Outline each Plasmodium ovale-infected red blood cell.
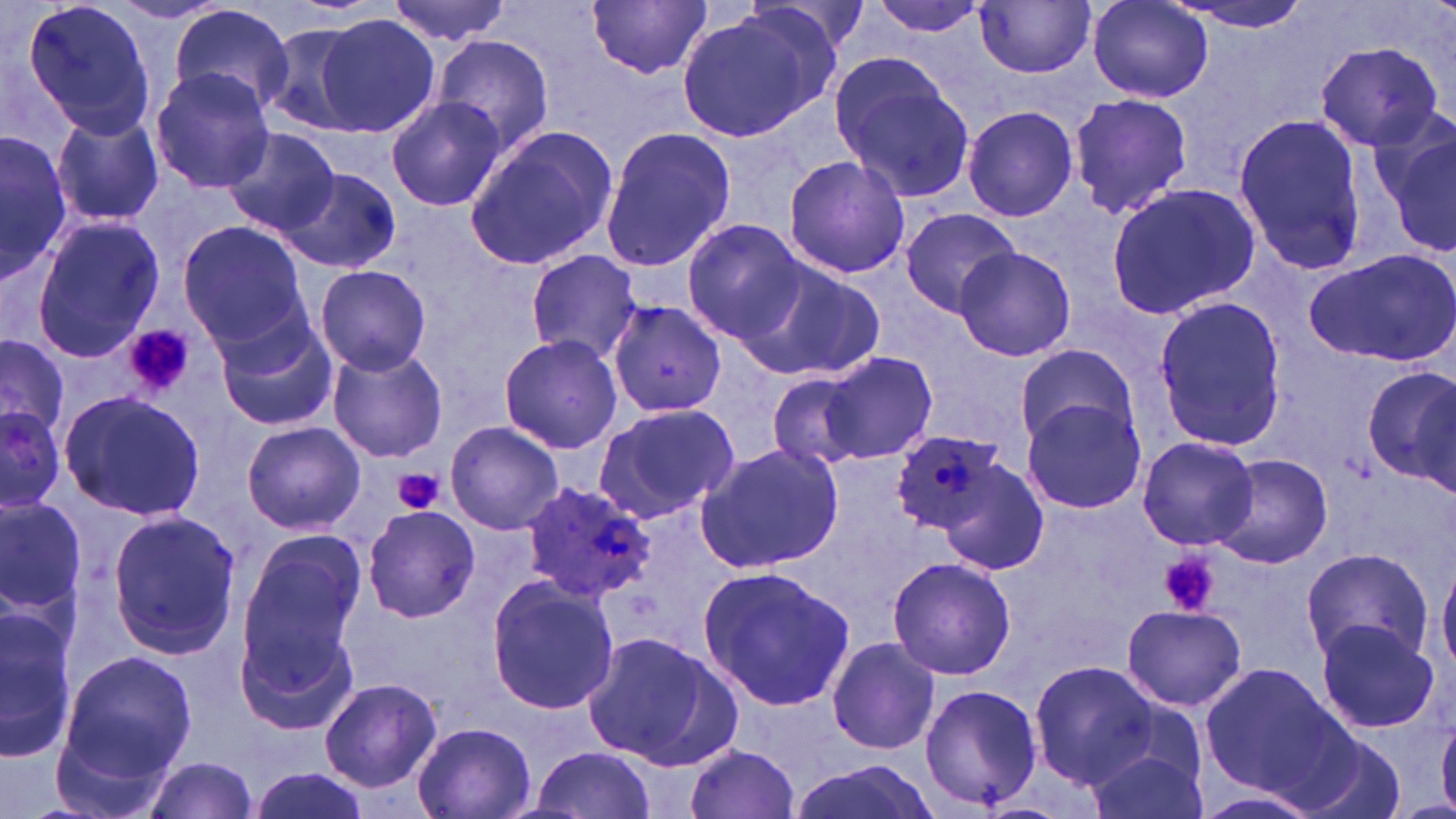
Approximate bounding boxes as (x1, y1, x2, y2) in pixels.
Plasmodium ovale-infected red blood cells: (521, 480, 657, 601).

slide-level diagnosis = Plasmodium ovale
platelet locations = approximate bounding boxes as (x1, y1, x2, y2) in pixels: (123, 325, 194, 397), (393, 469, 444, 515), (1158, 549, 1218, 618)
preparation = thin blood film
stain = May-Grünwald-Giemsa
uninfected red blood cell locations = approximate bounding boxes as (x1, y1, x2, y2) in pixels: (19, 0, 159, 142), (385, 0, 514, 45), (866, 0, 991, 38), (1170, 0, 1317, 37), (108, 1, 230, 24), (588, 1, 711, 80), (975, 1, 1097, 77), (1087, 1, 1212, 103), (167, 5, 295, 117), (674, 7, 840, 143), (314, 13, 442, 136), (257, 21, 376, 137), (433, 34, 555, 157), (1314, 40, 1445, 153), (829, 52, 975, 200), (152, 68, 274, 191), (1066, 92, 1193, 220), (385, 95, 509, 213), (962, 104, 1080, 222), (50, 108, 164, 228), (1229, 112, 1369, 279), (1375, 116, 1456, 255), (465, 123, 617, 271), (598, 125, 737, 273), (220, 126, 340, 237), (0, 129, 68, 283), (781, 156, 912, 279), (276, 167, 402, 274), (1104, 183, 1261, 320), (900, 206, 1022, 315), (28, 216, 164, 361), (177, 221, 306, 347), (683, 221, 808, 345), (951, 247, 1077, 362), (1304, 249, 1456, 368), (524, 250, 644, 363), (739, 256, 885, 382), (314, 264, 432, 375), (1152, 293, 1286, 448), (605, 299, 731, 420), (214, 314, 338, 432), (497, 334, 624, 454), (1, 335, 69, 446), (1014, 342, 1138, 453), (328, 346, 447, 463), (822, 352, 938, 463), (1365, 363, 1456, 496), (763, 371, 880, 472), (58, 389, 206, 523), (1019, 395, 1149, 517), (0, 402, 70, 516), (590, 403, 740, 527), (241, 421, 365, 534), (444, 421, 563, 535), (890, 431, 1008, 540), (1136, 434, 1259, 551), (695, 441, 843, 574), (1211, 453, 1333, 569), (939, 459, 1048, 576), (0, 498, 86, 613), (361, 503, 483, 623), (106, 511, 242, 658), (235, 536, 367, 673), (1300, 547, 1431, 666), (887, 556, 1018, 681), (1436, 556, 1456, 677), (698, 565, 856, 712), (485, 575, 620, 716), (235, 603, 361, 739), (0, 604, 76, 761), (1121, 604, 1247, 711), (1315, 618, 1442, 736), (582, 630, 740, 769), (826, 636, 941, 756), (59, 650, 194, 781), (1029, 661, 1158, 787), (1199, 661, 1351, 801), (319, 679, 442, 792), (916, 685, 1043, 810), (412, 722, 537, 819), (1289, 728, 1403, 819), (1084, 736, 1208, 819), (529, 743, 658, 818), (682, 743, 803, 819), (139, 756, 263, 819), (790, 760, 940, 819), (246, 767, 371, 819), (1188, 786, 1324, 819)
field of view = single
image size = 1456×819 pixels
magnification = 1000x
modality = optical microscopy